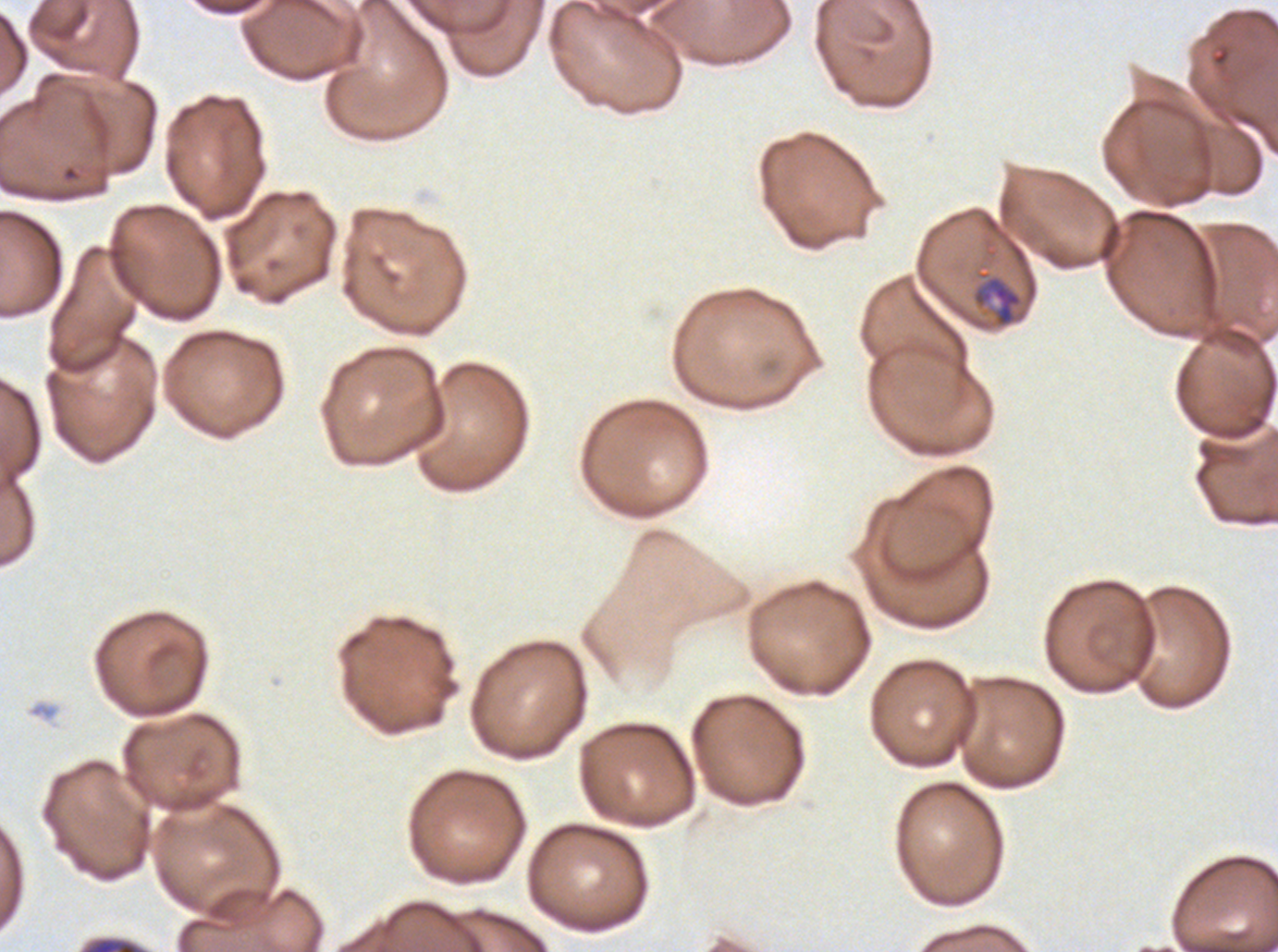 Approximate bounding rectangles given as corner coordinates in pixels from the top-left. Late-ring/early-trophozoite locations: (x1=972, y1=270, x2=1023, y2=328). A sub-image separated from a larger composite. Thin blood smear. Giemsa stain. Plasmodium falciparum from a patient in The Gambia, cultured ex vivo for 24 to 48 hours. Image is 1278×952 pixels.